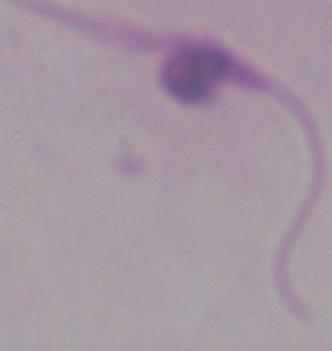
identification: Leishmania
modality: photomicrograph
magnification: 1000x